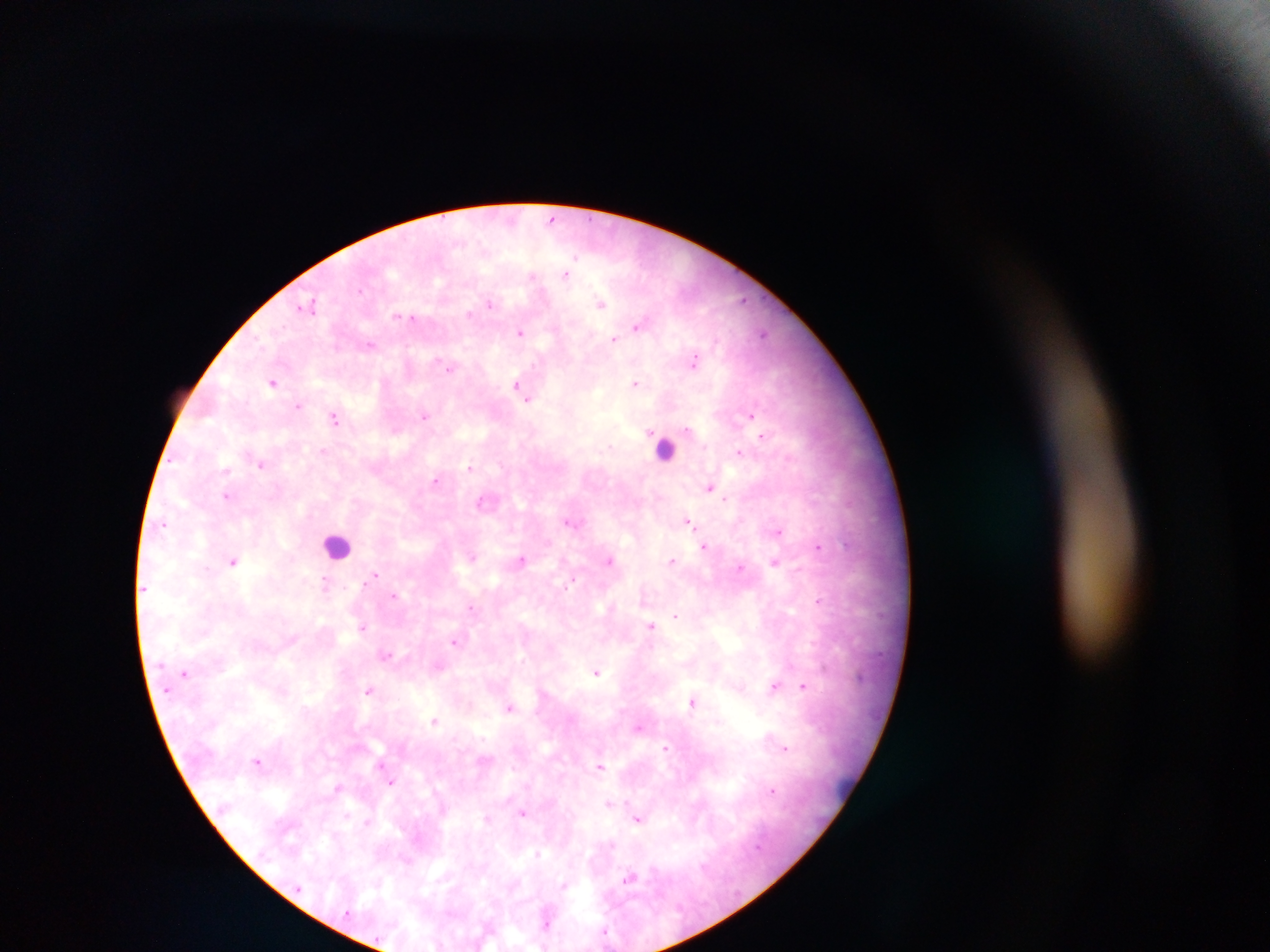

Approximate centers as [x, y] in pixels. Leukocyte locations: [667, 444], [337, 539]. Malaria parasite locations: [552, 218], [566, 275], [533, 276], [742, 301], [600, 303], [490, 304], [469, 313], [639, 325], [765, 332], [519, 333], [614, 339], [368, 344], [694, 364], [449, 368], [274, 382], [636, 382], [520, 388], [298, 406], [424, 415], [750, 415], [335, 418], [763, 434], [322, 451], [739, 451], [261, 464], [469, 467], [225, 469], [435, 479], [710, 486], [227, 496], [726, 500], [688, 520], [567, 522], [164, 524], [780, 531], [705, 546], [817, 547], [523, 559], [610, 560], [672, 560], [775, 561], [233, 562], [741, 567], [375, 576], [325, 584], [393, 596], [819, 599], [471, 608], [676, 616], [652, 627], [362, 628], [454, 642], [385, 653], [595, 672], [774, 687], [803, 687], [369, 689], [692, 702], [510, 708], [434, 720], [640, 726], [666, 748], [786, 748], [257, 761], [600, 767], [392, 783], [335, 787], [774, 789], [522, 813], [638, 820], [366, 822], [536, 852], [655, 868], [630, 876], [563, 884], [606, 930]. Image is 1270×952 pixels. Mobile-phone photograph taken through the microscope. Single field of view. Thick blood smear. Sample from Ghana.